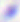
modality = micrograph
identification = Toxoplasma gondii
magnification = 400x